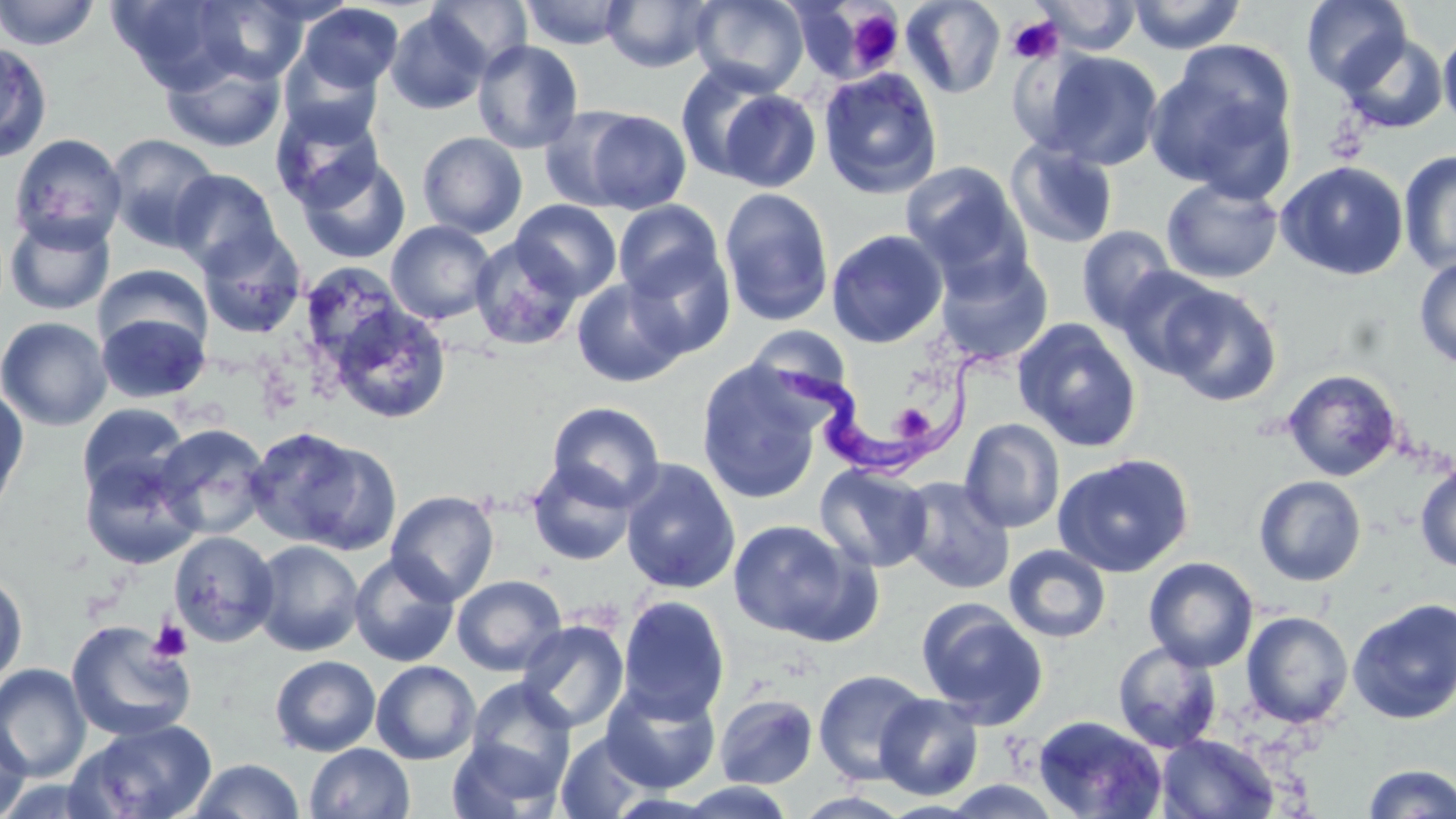

{
  "slide_level_diagnosis": "Trypanosoma brucei",
  "image_size": "1456×819 pixels",
  "field_of_view": "single",
  "magnification": "1000x",
  "trypanosoma_brucei_locations": "approximate bounding boxes as (x1, y1, x2, y2) in pixels: (767, 341, 1008, 481)",
  "platelet_locations": "approximate bounding boxes as (x1, y1, x2, y2) in pixels: (844, 8, 903, 73), (1007, 16, 1064, 64), (894, 401, 933, 443), (148, 618, 193, 663)",
  "modality": "optical microscopy",
  "stain": "May-Grünwald-Giemsa",
  "preparation": "thin blood smear",
  "uninfected_red_blood_cell_locations": "approximate bounding boxes as (x1, y1, x2, y2) in pixels: (0, 0, 101, 51), (109, 0, 245, 92), (691, 0, 810, 95), (900, 0, 1006, 99), (1032, 0, 1142, 55), (1127, 0, 1247, 54), (1301, 0, 1412, 92), (192, 1, 309, 84), (425, 1, 533, 74), (518, 1, 634, 49), (601, 1, 718, 72), (296, 3, 404, 94), (385, 8, 492, 114), (1439, 27, 1456, 132), (1337, 32, 1450, 134), (472, 39, 584, 154), (0, 40, 53, 163), (1148, 48, 1297, 194), (279, 49, 384, 146), (1040, 50, 1163, 169), (161, 51, 285, 153), (675, 62, 786, 182), (818, 67, 944, 199), (716, 88, 821, 192), (271, 103, 384, 211), (539, 107, 646, 211), (576, 108, 693, 215), (417, 131, 528, 238), (8, 132, 128, 251), (105, 133, 223, 251), (1005, 140, 1118, 251), (1398, 150, 1456, 274), (296, 154, 410, 265), (1276, 160, 1409, 281), (901, 162, 1031, 284), (168, 169, 283, 275), (1161, 177, 1284, 284), (719, 187, 835, 327), (511, 199, 622, 301), (613, 200, 725, 302), (3, 211, 116, 316), (385, 220, 497, 325), (1077, 226, 1178, 333), (195, 227, 308, 339), (827, 229, 948, 348), (469, 235, 582, 351), (626, 248, 736, 360), (934, 251, 1054, 367), (1414, 256, 1456, 368), (299, 261, 408, 372), (95, 264, 213, 356), (1113, 266, 1230, 379), (572, 277, 688, 388), (1155, 282, 1283, 407), (329, 304, 452, 425), (95, 309, 211, 404), (0, 316, 113, 431), (1011, 318, 1143, 452), (746, 325, 853, 408), (696, 362, 824, 504), (1281, 368, 1403, 482), (0, 383, 29, 520), (546, 402, 665, 510), (76, 403, 190, 504), (959, 418, 1065, 534), (152, 424, 271, 540), (247, 427, 398, 555), (79, 452, 203, 570), (1053, 453, 1195, 578), (527, 459, 639, 567), (619, 459, 741, 595), (815, 462, 933, 573), (1415, 464, 1456, 573), (1253, 475, 1366, 587), (898, 476, 1015, 595), (386, 489, 499, 606), (727, 518, 871, 643), (168, 531, 280, 647), (250, 539, 365, 656), (1004, 545, 1111, 643), (348, 552, 460, 667), (1143, 557, 1259, 672), (0, 569, 28, 690), (451, 574, 566, 675), (616, 595, 730, 723), (1347, 597, 1456, 725), (916, 599, 1049, 728), (1241, 610, 1354, 728), (516, 619, 629, 733), (66, 620, 196, 742), (1112, 641, 1223, 753), (270, 654, 381, 757), (371, 660, 480, 765), (0, 663, 91, 781), (813, 668, 932, 786), (465, 678, 577, 797), (601, 682, 721, 794), (714, 693, 819, 789), (875, 693, 984, 800), (1031, 715, 1168, 818), (0, 718, 31, 819), (73, 718, 218, 819), (555, 731, 657, 818), (1156, 733, 1279, 818), (447, 735, 564, 819), (306, 743, 415, 819), (188, 758, 304, 818), (1362, 763, 1455, 819), (935, 779, 1068, 818), (676, 782, 799, 818)"
}